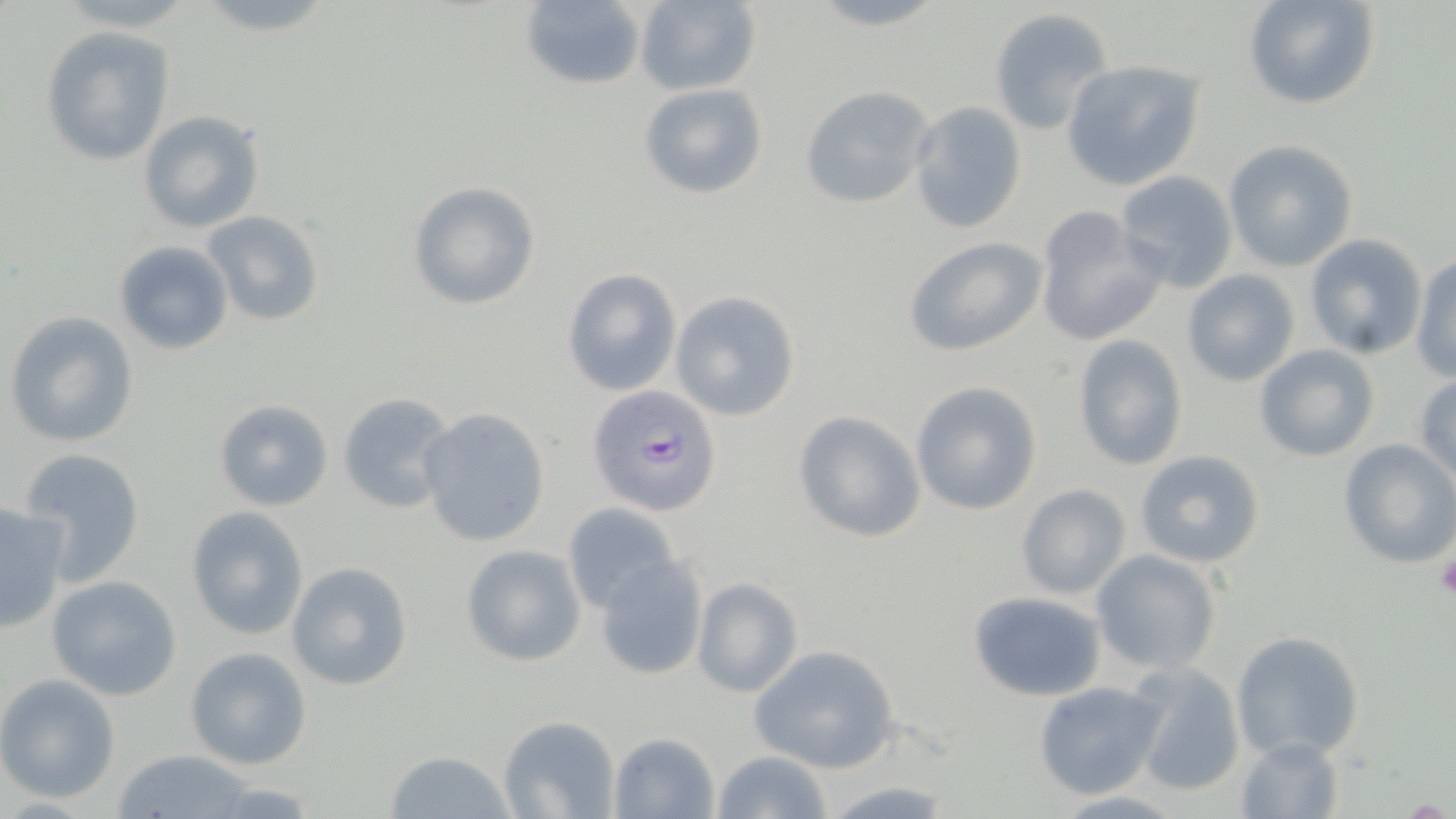
{
  "slide_level_diagnosis": "Plasmodium falciparum",
  "magnification": "1000x",
  "field_of_view": "one of a larger specimen",
  "uninfected_red_blood_cell_locations": "approximate bounding boxes as [x1, y1, x2, y2] in pixels: [194, 0, 338, 38], [633, 0, 761, 95], [803, 0, 952, 31], [1244, 0, 1380, 111], [519, 1, 649, 89], [987, 8, 1114, 136], [41, 26, 175, 167], [1061, 58, 1207, 191], [639, 83, 767, 201], [798, 86, 933, 209], [908, 100, 1027, 233], [139, 110, 264, 233], [1224, 140, 1357, 270], [1114, 169, 1239, 292], [405, 179, 542, 312], [1033, 206, 1167, 347], [203, 209, 325, 326], [1303, 232, 1431, 358], [902, 236, 1047, 356], [112, 239, 235, 355], [1410, 254, 1456, 381], [560, 268, 682, 396], [1181, 269, 1300, 388], [669, 291, 803, 422], [4, 311, 140, 447], [1071, 333, 1189, 470], [1252, 343, 1381, 462], [1413, 373, 1456, 484], [909, 380, 1043, 515], [336, 392, 456, 515], [213, 398, 334, 511], [417, 407, 551, 548], [793, 410, 928, 543], [1337, 439, 1455, 568], [16, 448, 147, 585], [1134, 449, 1267, 568], [1015, 484, 1133, 599], [0, 503, 71, 630], [562, 505, 680, 612], [184, 506, 309, 641], [460, 543, 585, 667], [1090, 549, 1224, 677], [593, 558, 707, 681], [286, 561, 414, 690], [46, 574, 184, 701], [691, 577, 805, 697], [968, 591, 1107, 701], [1230, 630, 1365, 764], [750, 644, 901, 773], [184, 647, 312, 770], [1125, 661, 1248, 797], [0, 674, 121, 804], [1032, 679, 1169, 801], [498, 714, 620, 819], [608, 732, 721, 818], [1236, 734, 1344, 818], [386, 749, 516, 819], [713, 749, 835, 819], [112, 750, 263, 819], [822, 779, 958, 816], [1053, 791, 1186, 819]",
  "image_size": "1456×819 pixels",
  "stain": "May-Grünwald-Giemsa",
  "plasmodium_falciparum_infected_red_blood_cell_locations": "approximate bounding boxes as [x1, y1, x2, y2] in pixels: [586, 384, 725, 516]",
  "preparation": "thin blood smear",
  "platelet_locations": "approximate bounding boxes as [x1, y1, x2, y2] in pixels: [1436, 553, 1456, 601]",
  "modality": "light microscopy"
}